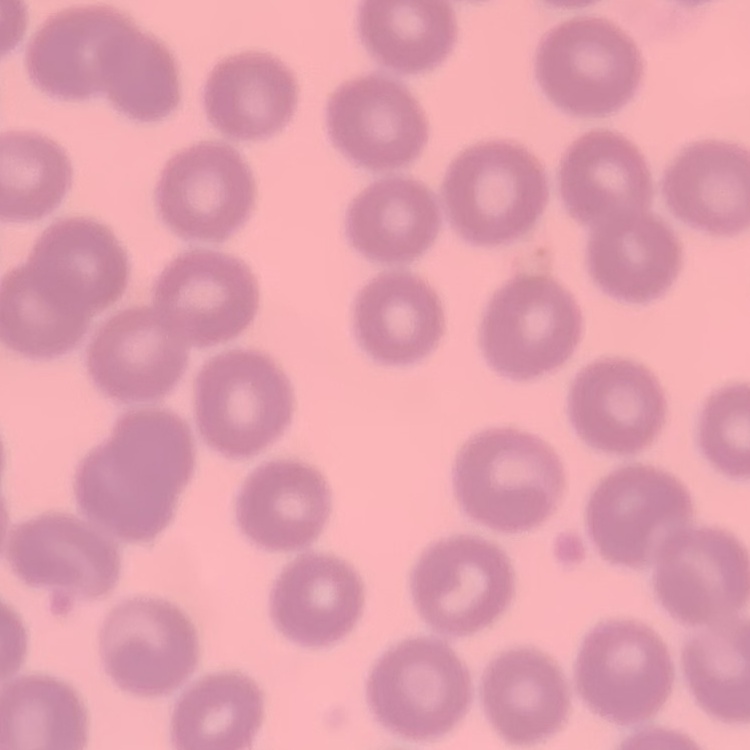
The erythrocytes show no rouleaux formation. Square crop of a larger photomicrograph. Field's or Giemsa stain. Thin blood smear.